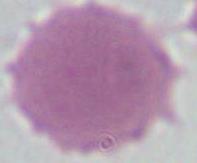
magnification = 1000x
identification = red blood cell
modality = photomicrograph